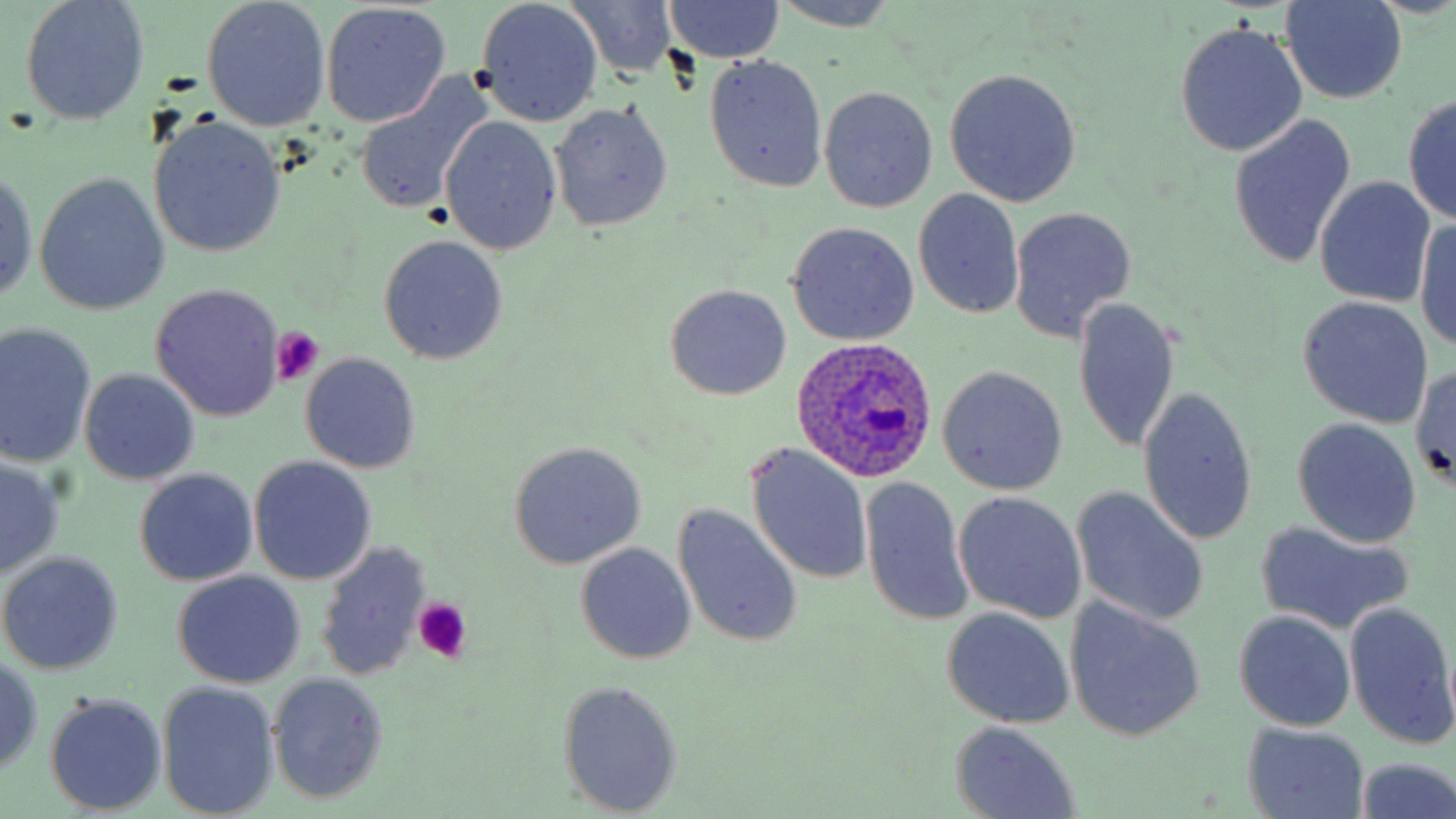
slide-level diagnosis = Plasmodium ovale
preparation = thin blood film
platelet locations = approximate bounding boxes as [x1, y1, x2, y2] in pixels: [268, 328, 323, 386], [412, 600, 469, 664]
image size = 1456×819 pixels
magnification = 1000x
Plasmodium ovale-infected red blood cell locations = approximate bounding boxes as [x1, y1, x2, y2] in pixels: [790, 337, 939, 482]
uninfected red blood cell locations = approximate bounding boxes as [x1, y1, x2, y2] in pixels: [19, 0, 150, 125], [564, 0, 679, 81], [663, 0, 785, 65], [1281, 0, 1405, 103], [200, 1, 333, 130], [476, 1, 602, 126], [769, 1, 902, 32], [322, 3, 452, 126], [1175, 21, 1307, 157], [704, 54, 829, 193], [944, 68, 1082, 207], [354, 72, 496, 215], [818, 86, 937, 213], [1403, 94, 1456, 222], [550, 100, 674, 231], [1229, 112, 1358, 270], [440, 116, 562, 255], [148, 117, 285, 257], [0, 168, 39, 304], [34, 174, 170, 314], [1314, 176, 1436, 306], [913, 188, 1025, 320], [1009, 206, 1137, 342], [1415, 218, 1456, 351], [786, 221, 920, 346], [377, 235, 508, 365], [150, 283, 285, 422], [665, 284, 792, 401], [1073, 297, 1181, 455], [1296, 297, 1434, 428], [0, 324, 97, 467], [300, 351, 421, 473], [1410, 363, 1455, 491], [938, 366, 1068, 494], [80, 369, 199, 485], [1137, 384, 1259, 547], [1290, 418, 1422, 547], [507, 442, 648, 570], [746, 444, 874, 587], [250, 456, 377, 585], [0, 459, 65, 579], [135, 470, 256, 585], [859, 478, 972, 628], [1071, 486, 1209, 626], [953, 492, 1088, 623], [672, 505, 804, 649], [1256, 520, 1415, 635], [315, 541, 432, 683], [576, 542, 697, 664], [0, 552, 124, 675], [173, 571, 306, 689], [1065, 600, 1206, 743], [1343, 601, 1456, 750], [941, 608, 1075, 728], [1233, 610, 1357, 731], [0, 653, 45, 772], [267, 672, 389, 802], [556, 678, 684, 817], [157, 681, 280, 819], [45, 694, 166, 815], [949, 722, 1082, 817], [1242, 725, 1368, 816], [1352, 758, 1456, 819]
field of view = single
modality = light microscopy
stain = May-Grünwald-Giemsa